Locate and identify every blood parasite.
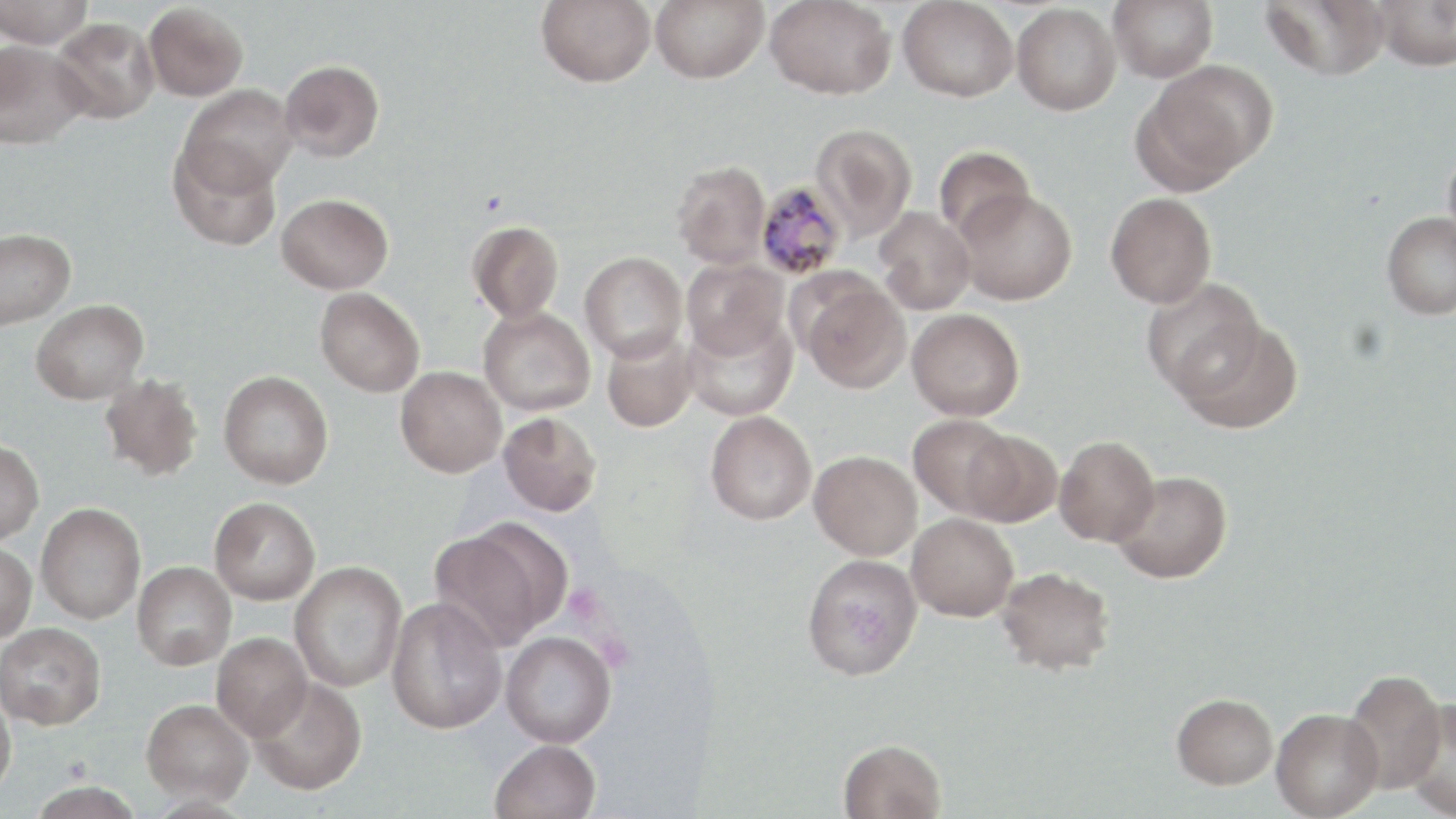
Approximate bounding boxes as [x1, y1, x2, y2] in pixels.
Plasmodium malariae-infected red blood cells: [755, 180, 848, 281].
No Plasmodium falciparum, Plasmodium ovale, Plasmodium vivax, Babesia divergens, or Trypanosoma brucei observed.

Summary:
  - Uninfected red blood cell locations: [0, 0, 93, 48], [536, 0, 656, 86], [651, 0, 769, 82], [765, 0, 896, 99], [899, 0, 1018, 102], [1108, 0, 1218, 82], [1261, 0, 1391, 81], [1373, 0, 1456, 71], [144, 3, 248, 101], [1012, 3, 1121, 115], [51, 16, 160, 124], [0, 40, 89, 149], [279, 60, 384, 162], [1138, 60, 1276, 188], [178, 84, 298, 194], [810, 123, 917, 240], [1442, 140, 1456, 256], [168, 141, 283, 252], [934, 145, 1034, 241], [671, 161, 771, 269], [955, 188, 1077, 305], [1106, 192, 1217, 308], [276, 193, 393, 294], [874, 207, 976, 315], [1382, 211, 1456, 320], [467, 220, 563, 324], [0, 228, 76, 329], [579, 251, 688, 362], [681, 258, 789, 360], [798, 277, 911, 393], [1141, 277, 1266, 400], [315, 287, 425, 397], [31, 299, 149, 404], [478, 306, 596, 415], [907, 308, 1025, 420], [682, 313, 798, 421], [1177, 319, 1303, 434], [601, 329, 699, 432], [395, 366, 507, 477], [219, 371, 334, 488], [99, 373, 205, 482], [705, 410, 817, 525], [499, 412, 602, 516], [907, 413, 1019, 519], [962, 429, 1062, 527], [1054, 435, 1160, 545], [0, 440, 44, 545], [809, 450, 922, 560], [1111, 470, 1232, 584], [209, 497, 320, 604], [36, 503, 145, 624], [906, 512, 1019, 621], [430, 524, 563, 651], [0, 542, 37, 642], [802, 553, 923, 680], [132, 561, 236, 669], [289, 561, 407, 692], [995, 566, 1115, 675], [385, 596, 507, 735], [0, 622, 106, 729], [500, 631, 616, 747], [212, 633, 312, 740], [1342, 670, 1448, 795], [248, 676, 367, 795], [0, 688, 17, 799], [1172, 693, 1277, 788], [1402, 697, 1455, 817], [142, 699, 252, 804], [1271, 708, 1383, 819], [489, 739, 601, 819], [838, 739, 945, 819], [27, 781, 145, 818]
  - Slide-level diagnosis: Plasmodium malariae
  - Preparation: thin blood film
  - Image size: 1456×819 pixels
  - Stain: May-Grünwald-Giemsa
  - Field of view: single
  - Magnification: 1000x
  - Modality: light microscopy